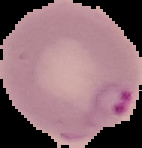
Summary:
  - Preparation: thin blood film
  - Result: Plasmodium parasites detected
  - Image type: segmented cell region on a black background
  - Image size: 142×148 pixels